State which cell type is depicted.
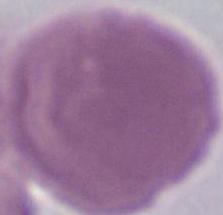
An erythrocyte.

1000x magnification. Micrograph.